Outline each blood parasite and name the species.
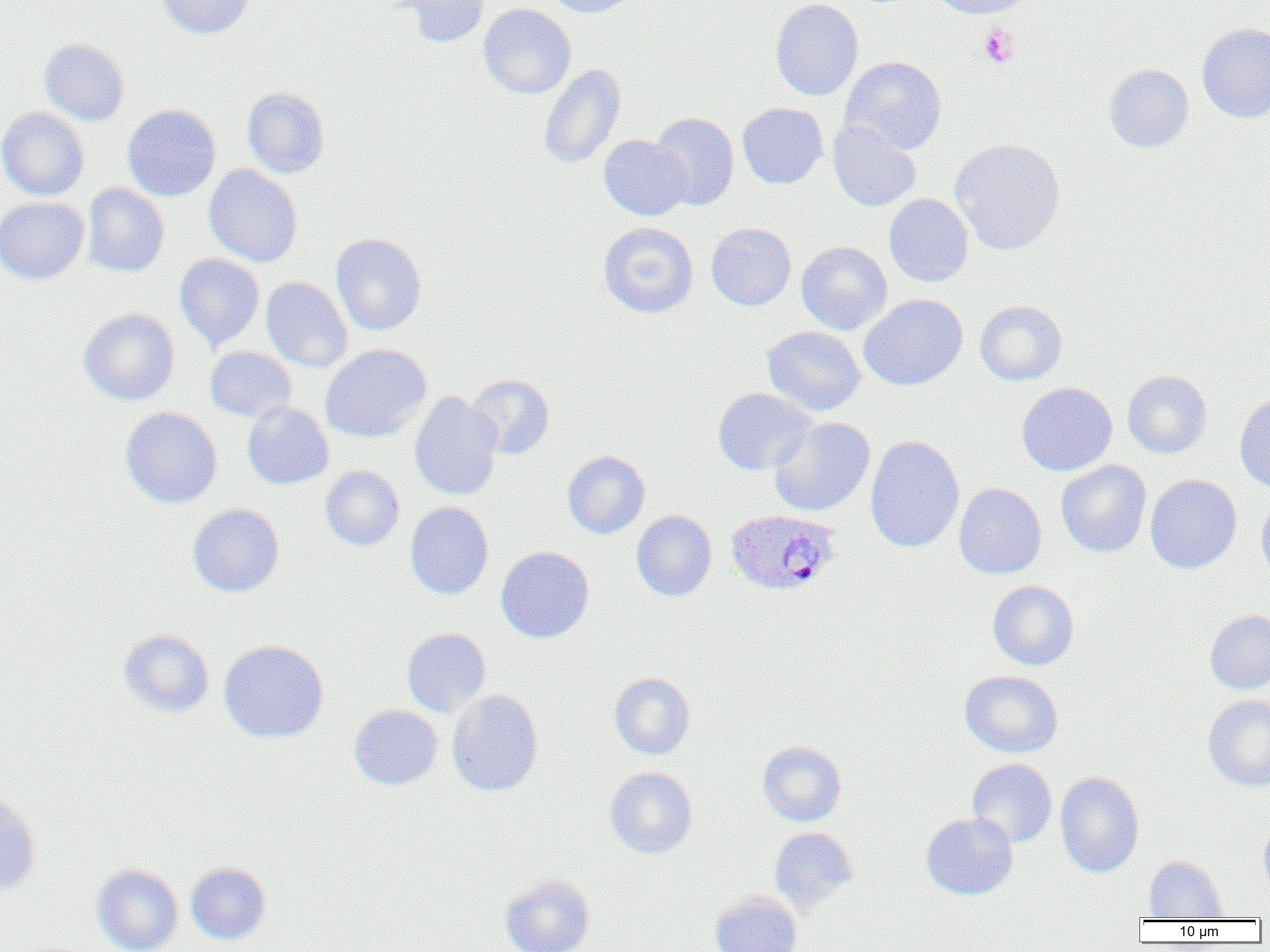

Approximate bounding boxes as named x1/y1/x2/y2 corners in pixels.
Plasmodium ovale-infected red blood cells: (x1=725, y1=509, x2=842, y2=596).
No Plasmodium falciparum, Plasmodium malariae, Plasmodium vivax, Babesia divergens, or Trypanosoma brucei observed.

Uninfected red blood cell locations: (x1=156, y1=0, x2=253, y2=39), (x1=388, y1=0, x2=491, y2=47), (x1=542, y1=0, x2=642, y2=17), (x1=770, y1=0, x2=864, y2=101), (x1=926, y1=0, x2=1037, y2=19), (x1=478, y1=3, x2=576, y2=100), (x1=1197, y1=24, x2=1270, y2=123), (x1=39, y1=39, x2=129, y2=125), (x1=840, y1=56, x2=947, y2=155), (x1=539, y1=64, x2=626, y2=169), (x1=1104, y1=64, x2=1193, y2=152), (x1=242, y1=87, x2=330, y2=178), (x1=737, y1=103, x2=828, y2=189), (x1=122, y1=104, x2=220, y2=201), (x1=0, y1=107, x2=89, y2=201), (x1=650, y1=113, x2=739, y2=211), (x1=827, y1=120, x2=921, y2=212), (x1=598, y1=136, x2=691, y2=220), (x1=949, y1=139, x2=1066, y2=255), (x1=204, y1=165, x2=303, y2=267), (x1=82, y1=184, x2=169, y2=277), (x1=884, y1=194, x2=973, y2=286), (x1=0, y1=197, x2=89, y2=285), (x1=598, y1=222, x2=698, y2=318), (x1=706, y1=222, x2=796, y2=311), (x1=330, y1=233, x2=426, y2=336), (x1=796, y1=241, x2=892, y2=335), (x1=175, y1=254, x2=264, y2=350), (x1=261, y1=277, x2=353, y2=373), (x1=859, y1=294, x2=968, y2=391), (x1=975, y1=300, x2=1067, y2=385), (x1=78, y1=308, x2=180, y2=406), (x1=762, y1=326, x2=865, y2=416), (x1=321, y1=344, x2=432, y2=443), (x1=205, y1=347, x2=296, y2=422), (x1=1122, y1=370, x2=1212, y2=458), (x1=465, y1=374, x2=554, y2=459), (x1=1016, y1=382, x2=1117, y2=476), (x1=712, y1=388, x2=817, y2=475), (x1=409, y1=392, x2=503, y2=500), (x1=1235, y1=392, x2=1270, y2=493), (x1=242, y1=402, x2=333, y2=490), (x1=121, y1=407, x2=222, y2=508), (x1=768, y1=416, x2=875, y2=517), (x1=865, y1=436, x2=964, y2=553), (x1=562, y1=451, x2=650, y2=539), (x1=1056, y1=460, x2=1152, y2=557), (x1=320, y1=465, x2=404, y2=550), (x1=1145, y1=474, x2=1242, y2=574), (x1=954, y1=483, x2=1046, y2=579), (x1=1256, y1=494, x2=1270, y2=583), (x1=405, y1=502, x2=494, y2=599), (x1=187, y1=504, x2=284, y2=597), (x1=631, y1=511, x2=717, y2=601), (x1=496, y1=546, x2=594, y2=643), (x1=987, y1=580, x2=1079, y2=670), (x1=1204, y1=610, x2=1270, y2=694), (x1=402, y1=628, x2=491, y2=717), (x1=117, y1=629, x2=214, y2=718), (x1=218, y1=640, x2=329, y2=743), (x1=959, y1=670, x2=1063, y2=757), (x1=609, y1=673, x2=695, y2=759), (x1=446, y1=690, x2=543, y2=797), (x1=1202, y1=695, x2=1270, y2=791), (x1=348, y1=705, x2=443, y2=790), (x1=757, y1=740, x2=847, y2=827), (x1=967, y1=759, x2=1057, y2=848), (x1=604, y1=767, x2=697, y2=859), (x1=1055, y1=771, x2=1144, y2=878), (x1=0, y1=790, x2=42, y2=897), (x1=921, y1=812, x2=1018, y2=900), (x1=1258, y1=814, x2=1270, y2=900), (x1=769, y1=827, x2=859, y2=912), (x1=1144, y1=855, x2=1226, y2=920), (x1=185, y1=862, x2=271, y2=944), (x1=91, y1=864, x2=184, y2=952), (x1=500, y1=874, x2=595, y2=952), (x1=710, y1=890, x2=801, y2=952). Platelet locations: (x1=977, y1=24, x2=1019, y2=68). Slide-level diagnosis: Plasmodium ovale. Light microscopy. 1000x magnification. Thin blood smear. One field of a larger specimen. Image is 1270×952 pixels.